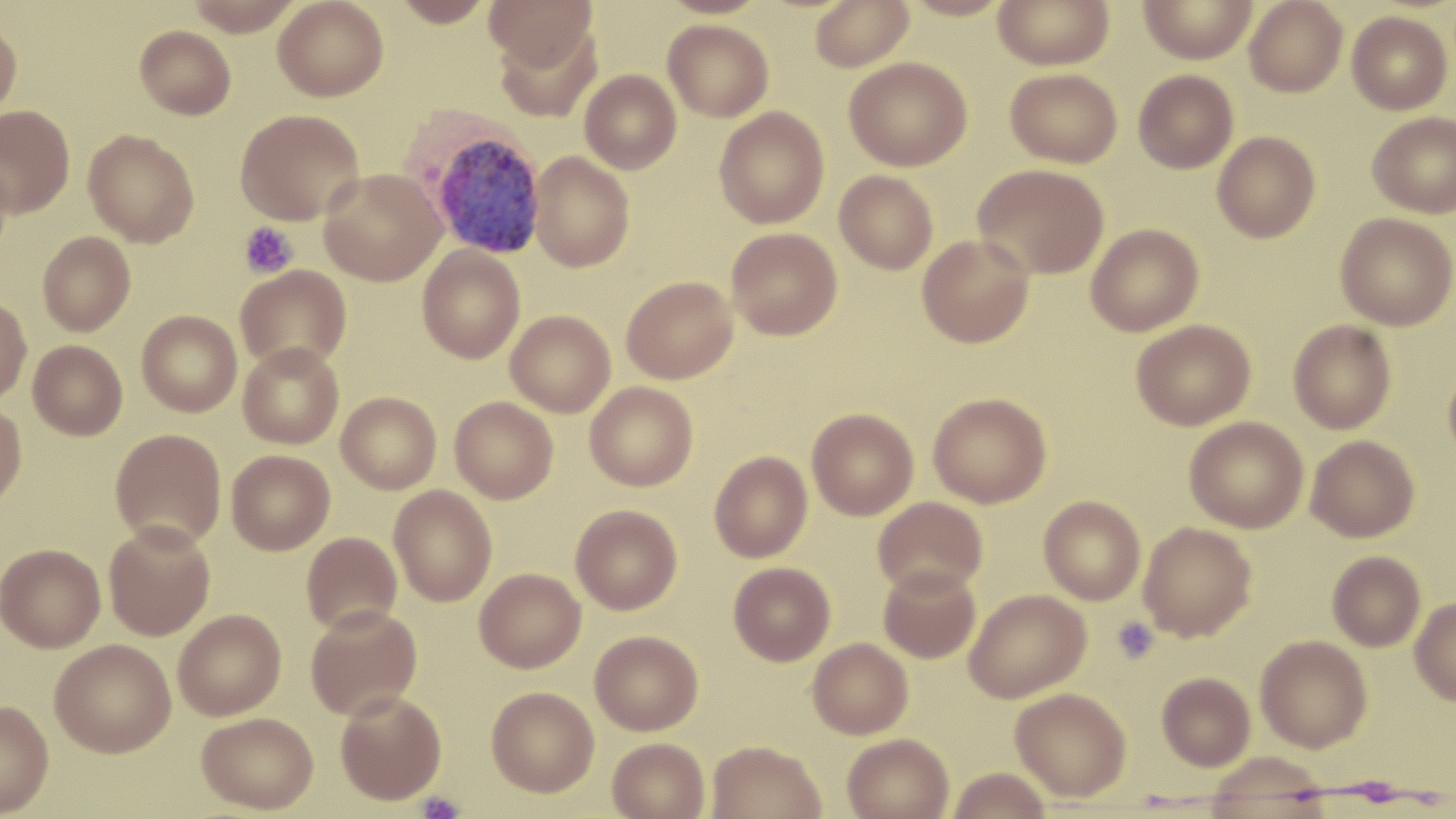

slide-level diagnosis = Plasmodium vivax
image size = 1456×819 pixels
field of view = single
modality = optical microscopy
magnification = 1000x
stain = May-Grünwald-Giemsa
uninfected red blood cell locations = approximate bounding boxes as (x1,y1)-(x2,y2) corner pairs in pixels: (184,0)-(306,36), (273,0)-(389,101), (391,0)-(495,27), (486,0)-(597,73), (809,0)-(914,72), (899,0)-(1015,21), (993,0)-(1115,70), (1244,0)-(1348,97), (1138,1)-(1259,64), (1347,10)-(1452,114), (0,19)-(22,118), (495,19)-(603,123), (663,19)-(774,122), (135,25)-(236,119), (844,56)-(972,171), (1005,68)-(1123,168), (580,69)-(681,174), (1134,70)-(1238,174), (0,105)-(75,216), (714,106)-(830,229), (235,109)-(364,225), (1367,111)-(1456,217), (83,129)-(199,247), (1212,131)-(1320,243), (529,151)-(635,272), (973,164)-(1110,279), (319,169)-(445,286), (834,170)-(939,274), (1335,213)-(1456,330), (1086,223)-(1204,336), (726,227)-(842,340), (38,231)-(136,336), (917,235)-(1034,348), (417,245)-(525,364), (236,265)-(351,373), (621,276)-(738,385), (0,296)-(31,405), (137,310)-(242,416), (505,310)-(615,417), (1131,319)-(1256,430), (1288,320)-(1397,434), (28,340)-(128,440), (238,342)-(344,449), (1444,360)-(1456,470), (585,381)-(698,491), (336,392)-(442,494), (928,392)-(1051,508), (449,396)-(558,503), (0,402)-(27,511), (807,408)-(919,520), (1184,417)-(1309,533), (110,428)-(226,549), (1306,435)-(1419,542), (226,450)-(335,555), (710,451)-(813,562), (389,485)-(497,606), (1038,495)-(1146,605), (873,496)-(988,597), (570,504)-(682,614), (1138,521)-(1257,642), (103,522)-(215,641), (301,532)-(403,635), (1,543)-(105,652), (1327,551)-(1425,651), (729,562)-(835,665), (878,566)-(981,663), (475,568)-(586,673), (964,589)-(1091,703), (1410,598)-(1456,705), (305,605)-(423,720), (172,609)-(286,720), (590,630)-(703,735), (1255,635)-(1372,752), (807,637)-(914,739), (49,638)-(176,756), (1157,672)-(1255,771), (486,686)-(599,797), (1010,687)-(1131,802), (335,690)-(447,805), (0,699)-(54,816), (196,711)-(319,813), (842,733)-(954,819), (607,738)-(710,819), (707,740)-(827,819), (947,767)-(1052,819)
Plasmodium vivax-infected red blood cell locations = approximate bounding boxes as (x1,y1)-(x2,y2) corner pairs in pixels: (423,125)-(546,259)
preparation = thin blood smear
platelet locations = approximate bounding boxes as (x1,y1)-(x2,y2) corner pairs in pixels: (239,222)-(297,279), (1111,617)-(1160,664), (416,792)-(465,819)